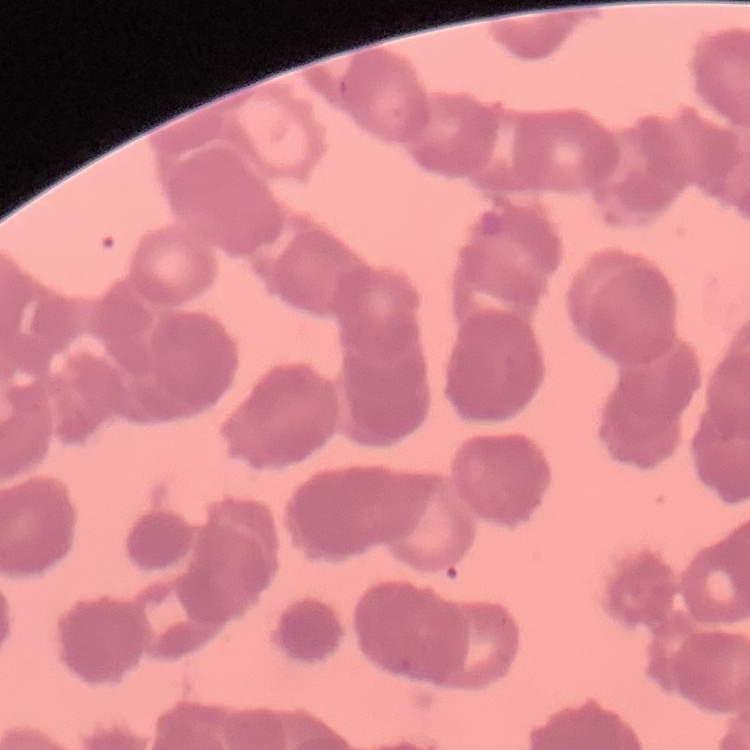
Summary:
  - Red blood cell morphology: rouleaux formation
  - Stain: Field's or Giemsa
  - Image type: square crop of a larger photomicrograph
  - Preparation: thin blood film